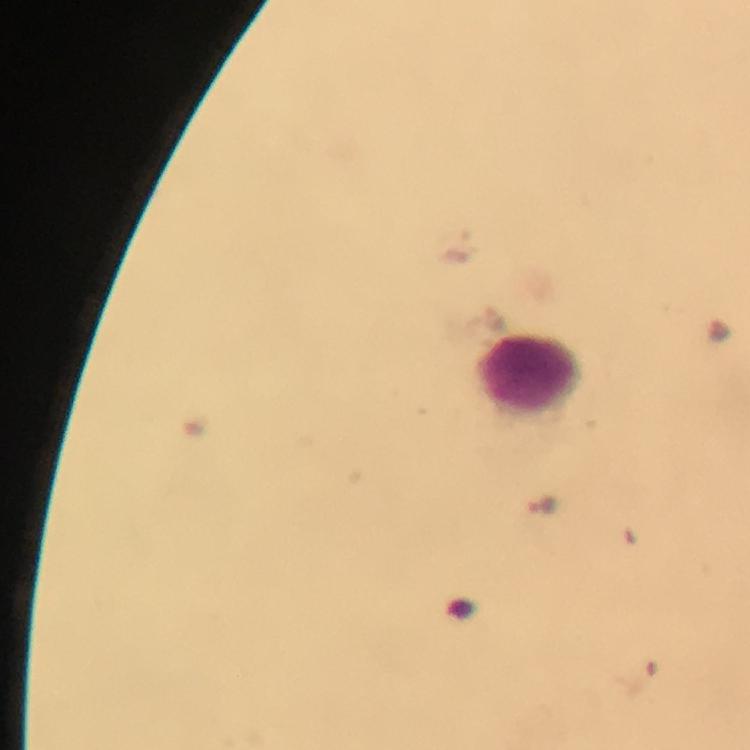 Approximate centers as [x, y] in pixels. Malaria parasite locations: [461, 245], [493, 316], [542, 506]. Leukocyte locations: [529, 375]. Image is 750×750 pixels. Immersion oil applied. Thick blood smear. Giemsa-stained preparation. Cropped region of a single field of view. From a diagnostic examination for malaria. Smartphone photograph taken through a microscope. 100x magnification.